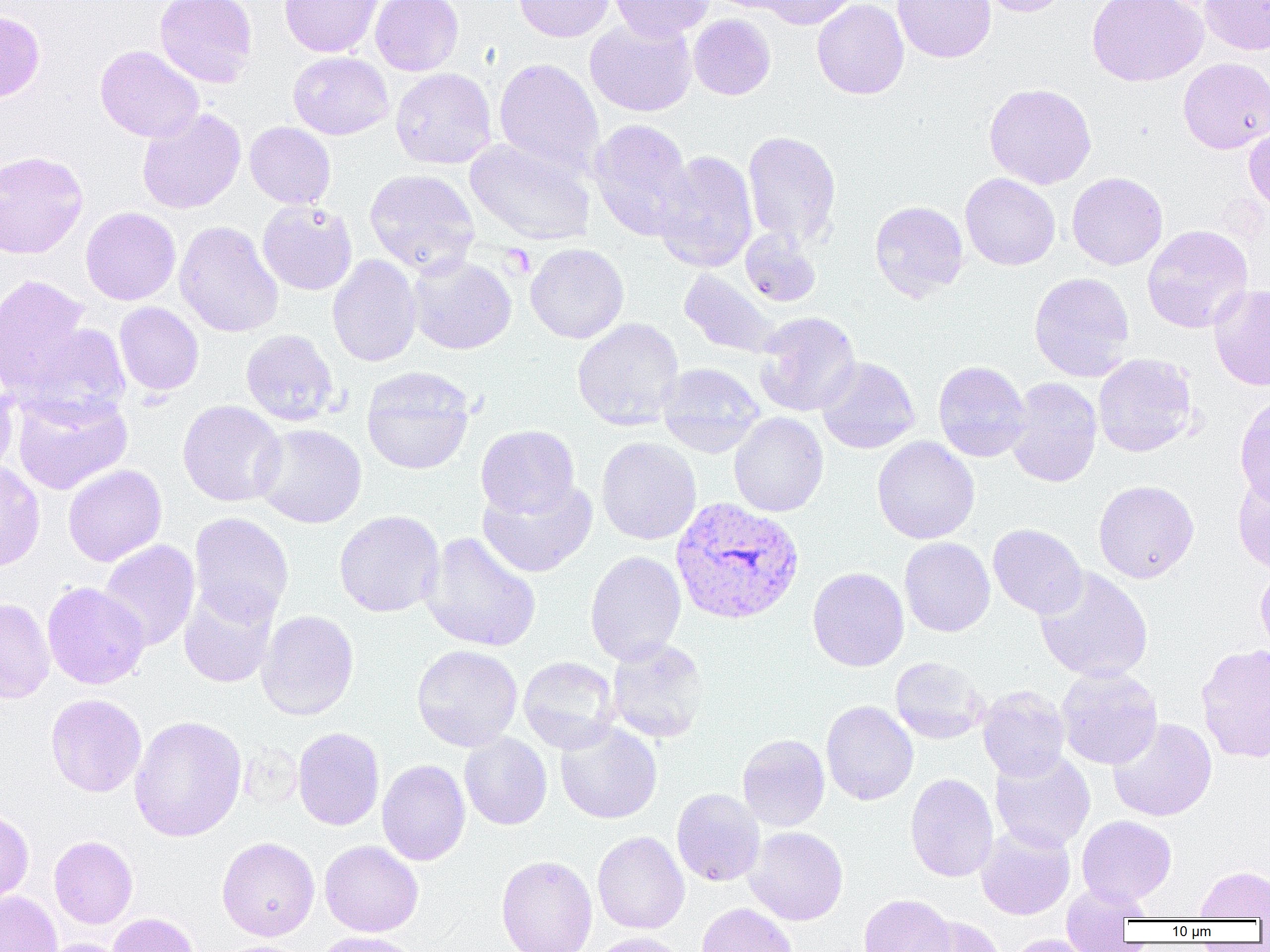

Summary:
  - Coordinate format: approximate bounding boxes as (x1,y1)-(x2,y2) corner pairs in pixels
  - Uninfected red blood cell locations: (154,0)-(257,88), (279,0)-(383,57), (370,0)-(464,75), (513,0)-(615,42), (609,0)-(714,41), (705,0)-(803,14), (755,0)-(860,29), (812,0)-(909,100), (892,0)-(996,63), (972,0)-(1075,17), (1086,0)-(1208,87), (1200,0)-(1270,55), (0,9)-(45,103), (688,14)-(776,100), (584,17)-(697,117), (95,45)-(204,142), (288,51)-(393,140), (1178,57)-(1270,154), (494,58)-(605,176), (390,68)-(497,169), (984,82)-(1097,190), (137,107)-(246,214), (590,119)-(694,240), (1244,120)-(1270,215), (244,122)-(336,209), (743,130)-(841,247), (464,139)-(595,244), (0,150)-(89,259), (654,150)-(758,272), (364,169)-(480,274), (1067,172)-(1168,270), (960,173)-(1060,271), (257,200)-(358,295), (869,200)-(969,301), (80,206)-(180,305), (174,221)-(283,338), (1142,225)-(1253,334), (740,228)-(821,307), (525,243)-(629,344), (327,255)-(421,367), (407,255)-(517,355), (679,269)-(783,359), (1029,272)-(1135,382), (0,274)-(92,392), (1209,285)-(1270,391), (115,302)-(204,396), (754,312)-(861,417), (572,317)-(685,430), (18,322)-(132,422), (240,328)-(340,426), (1093,353)-(1198,458), (816,356)-(920,454), (933,361)-(1030,462), (657,362)-(764,457), (362,367)-(475,475), (0,372)-(17,478), (1005,377)-(1102,487), (10,389)-(133,494), (1235,395)-(1270,505), (177,400)-(286,507), (729,412)-(828,517), (252,423)-(366,528), (475,424)-(580,519), (872,436)-(980,544), (596,437)-(701,545), (0,460)-(45,573), (62,464)-(167,566), (1233,469)-(1270,574), (478,477)-(597,577), (1093,480)-(1199,583), (334,510)-(445,617), (189,512)-(294,624), (988,524)-(1087,618), (420,531)-(541,652), (900,537)-(995,637), (98,540)-(200,651), (584,551)-(686,664), (1255,564)-(1270,658), (807,567)-(909,671), (1034,567)-(1154,683), (42,582)-(150,689), (178,584)-(279,689), (0,597)-(55,703), (257,610)-(359,721), (606,638)-(709,743), (1196,643)-(1270,763), (412,645)-(523,751), (518,656)-(621,753), (890,657)-(987,743), (1056,666)-(1162,770), (977,686)-(1070,781), (45,693)-(146,797), (821,701)-(918,806), (129,715)-(247,842), (1108,717)-(1217,821), (554,720)-(662,824), (292,727)-(385,830), (459,733)-(552,830), (737,733)-(830,831), (990,749)-(1095,853), (376,759)-(470,866), (905,772)-(999,882), (671,788)-(765,887), (0,809)-(34,905), (1077,815)-(1177,907), (976,825)-(1075,920), (745,826)-(848,925), (592,831)-(690,934), (49,836)-(137,928), (217,836)-(320,940), (320,841)-(423,937), (496,855)-(597,952), (1195,865)-(1270,919), (1061,883)-(1146,950), (0,890)-(61,952), (859,894)-(956,952), (695,903)-(799,952), (108,912)-(201,952), (908,915)-(1005,952), (311,931)-(420,952), (589,931)-(690,952), (1006,934)-(1098,952), (36,938)-(134,952), (218,940)-(310,952)
  - Plasmodium vivax-infected red blood cell locations: (670,496)-(805,625)
  - Platelet locations: (501,244)-(536,278)
  - Slide-level diagnosis: Plasmodium vivax
  - Image size: 1270×952 pixels
  - Modality: light microscopy
  - Field of view: one of a larger specimen
  - Magnification: 1000x
  - Preparation: thin blood film